Classify this cell by malaria status.
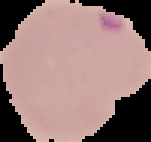
It is parasitized.

image type = segmented cell region on a black background
preparation = thin blood film
image size = 151×142 pixels